Give the extent of all Plasmodium malariae-infected red blood cells.
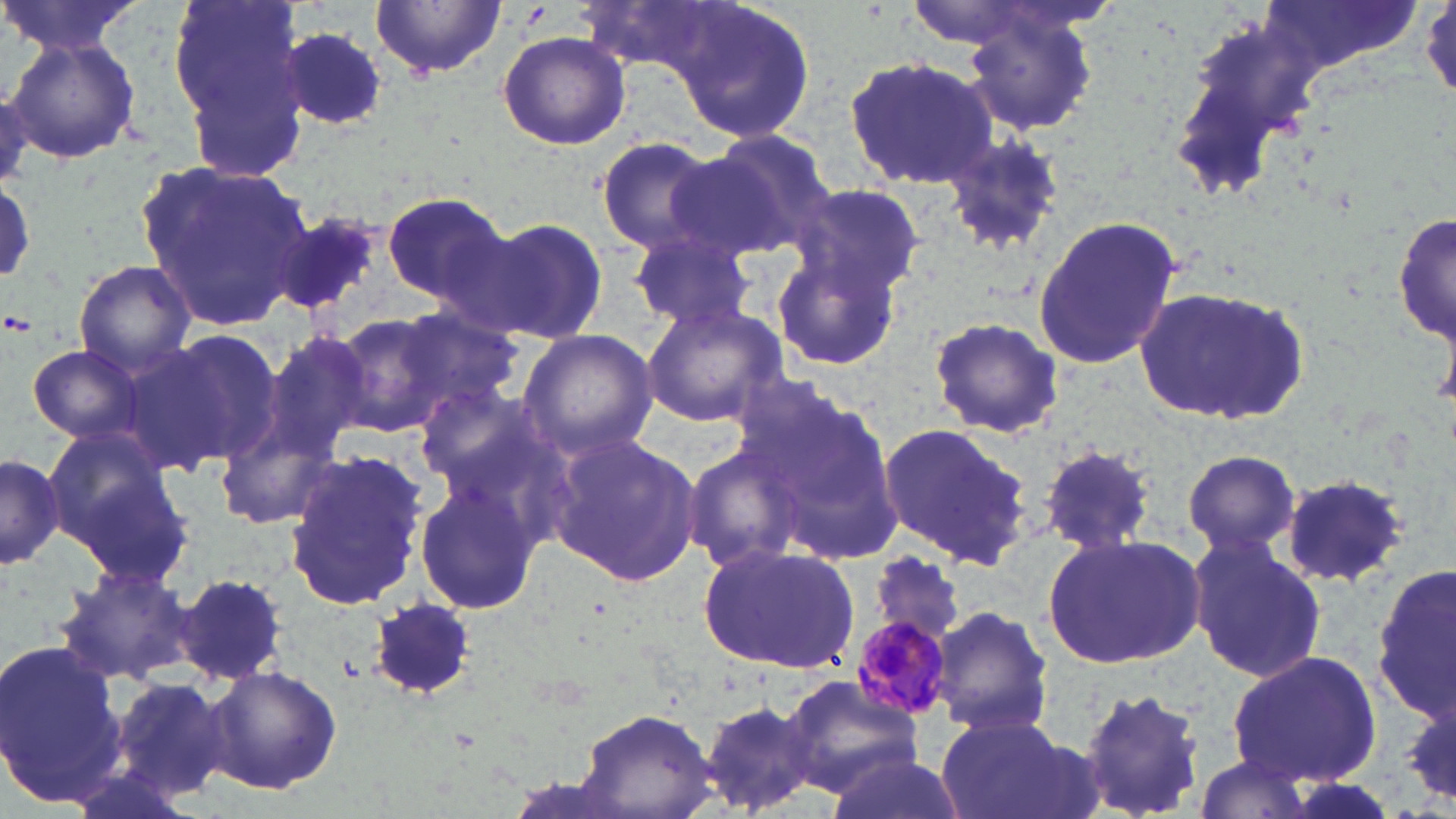

Approximate bounding boxes as (x1,y1)-(x2,y2) corner pairs in pixels.
Plasmodium malariae-infected red blood cells: (849,612)-(957,722).

slide-level diagnosis = Plasmodium malariae
image size = 1456×819 pixels
uninfected red blood cell locations = approximate bounding boxes as (x1,y1)-(x2,y2) corner pairs in pixels: (2,0)-(149,56), (166,0)-(310,174), (899,0)-(1051,49), (1254,0)-(1426,78), (372,1)-(505,78), (671,1)-(817,144), (956,7)-(1102,138), (1166,19)-(1324,203), (279,28)-(390,130), (496,30)-(631,151), (5,34)-(142,165), (843,55)-(999,189), (689,128)-(840,259), (937,131)-(1064,258), (592,135)-(729,256), (138,160)-(314,328), (0,178)-(35,292), (793,180)-(927,294), (381,191)-(512,306), (1394,201)-(1454,358), (268,210)-(383,320), (469,215)-(610,342), (1030,215)-(1184,371), (627,227)-(759,334), (770,247)-(905,371), (71,260)-(194,376), (1135,285)-(1311,426), (640,301)-(790,427), (391,308)-(523,423), (329,312)-(448,435), (926,314)-(1064,439), (126,330)-(283,474), (258,330)-(374,460), (517,330)-(660,462), (25,343)-(151,446), (746,377)-(909,564), (409,384)-(559,508), (213,417)-(343,531), (878,422)-(1033,570), (41,427)-(191,583), (547,432)-(703,587), (681,441)-(812,577), (1035,441)-(1160,558), (1181,447)-(1302,559), (0,450)-(65,571), (283,452)-(427,613), (1279,473)-(1411,589), (413,474)-(544,618), (1041,532)-(1206,671), (1185,534)-(1325,684), (697,542)-(858,672), (871,552)-(965,645), (1374,564)-(1455,724), (55,565)-(196,687), (178,575)-(288,683), (371,599)-(476,699), (930,605)-(1055,736), (0,641)-(125,803), (1226,649)-(1384,788), (206,665)-(342,796), (783,675)-(921,793), (113,676)-(228,796), (1074,686)-(1208,819), (1404,690)-(1456,808), (693,696)-(823,816), (579,707)-(720,818), (933,714)-(1082,819), (820,749)-(960,819), (1191,755)-(1317,816)
modality = light microscopy
stain = May-Grünwald-Giemsa
magnification = 1000x
field of view = single
preparation = thin blood smear